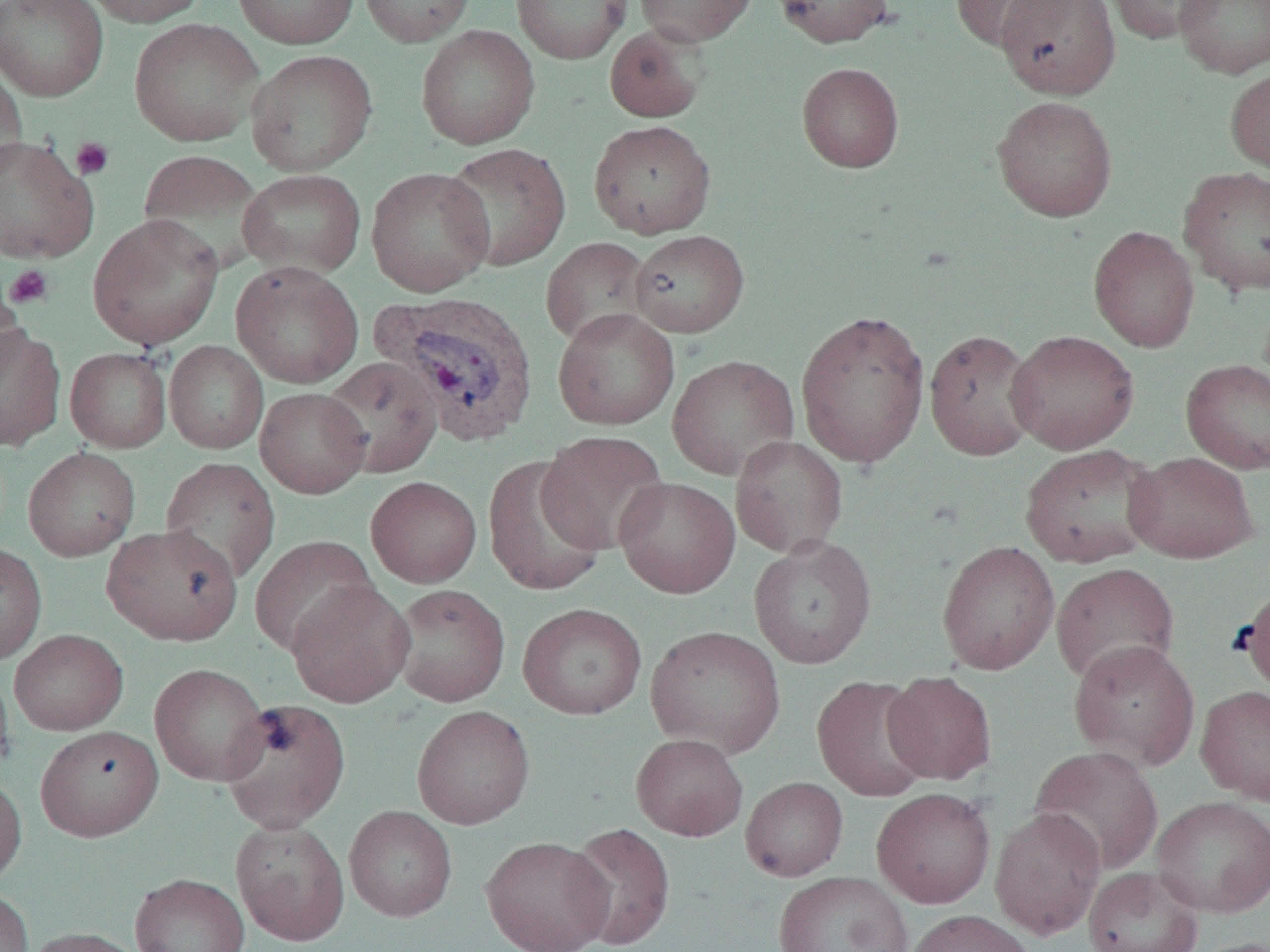

Approximate bounding boxes as (x1, y1, x2, y2) in pixels. Plasmodium vivax-infected red blood cell locations: (373, 290, 542, 446). Platelet locations: (71, 137, 114, 180), (4, 264, 54, 309). Uninfected red blood cell locations: (0, 0, 109, 102), (81, 0, 211, 27), (232, 0, 360, 49), (357, 0, 475, 47), (512, 0, 630, 64), (634, 0, 756, 46), (771, 0, 893, 48), (950, 0, 1072, 52), (996, 0, 1121, 99), (1103, 0, 1219, 45), (1174, 0, 1270, 79), (129, 18, 264, 147), (416, 25, 540, 149), (604, 25, 709, 123), (246, 49, 377, 176), (0, 58, 27, 180), (796, 62, 904, 173), (1225, 66, 1270, 177), (992, 96, 1118, 222), (589, 119, 716, 238), (0, 134, 99, 264), (440, 142, 571, 272), (137, 149, 268, 273), (1178, 165, 1270, 296), (366, 166, 495, 297), (238, 168, 366, 279), (87, 213, 224, 350), (1088, 225, 1199, 352), (629, 230, 749, 337), (540, 237, 653, 348), (230, 261, 364, 388), (0, 278, 27, 386), (552, 307, 680, 430), (794, 308, 931, 468), (0, 322, 66, 451), (923, 329, 1040, 460), (1005, 329, 1139, 454), (164, 341, 268, 454), (65, 347, 172, 452), (667, 354, 800, 480), (321, 356, 443, 477), (1180, 358, 1270, 473), (254, 386, 371, 498), (537, 430, 669, 554), (730, 436, 848, 558), (1019, 444, 1161, 568), (23, 446, 140, 561), (1124, 452, 1260, 563), (482, 455, 608, 597), (159, 456, 281, 585), (365, 476, 482, 587), (614, 476, 740, 598), (102, 524, 243, 646), (250, 535, 377, 656), (749, 535, 877, 669), (937, 540, 1060, 675), (0, 542, 47, 665), (1051, 562, 1180, 686), (285, 580, 415, 708), (1238, 583, 1270, 697), (390, 584, 510, 707), (517, 602, 647, 720), (645, 625, 786, 758), (9, 629, 129, 735), (1068, 640, 1200, 771), (0, 662, 14, 776), (149, 663, 271, 786), (883, 671, 996, 784), (812, 675, 934, 801), (1195, 685, 1270, 805), (220, 698, 351, 833), (412, 705, 535, 829), (34, 724, 164, 841), (631, 732, 748, 841), (1030, 745, 1164, 875), (0, 773, 27, 888), (741, 776, 848, 881), (872, 787, 996, 908), (1150, 795, 1270, 918), (344, 805, 457, 922), (990, 806, 1106, 939), (230, 819, 350, 945), (565, 822, 676, 950), (480, 835, 614, 952), (1083, 865, 1204, 952), (773, 871, 913, 952), (129, 872, 250, 952), (0, 887, 34, 952), (903, 909, 1036, 952), (22, 927, 147, 952), (1187, 937, 1270, 952). Slide-level diagnosis: Plasmodium vivax. Optical microscopy. Image is 1270×952 pixels. Single field of view. Thin blood smear. Captured at 1000x magnification.